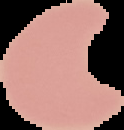
Image is 124×130 pixels. Result: negative for malaria parasites. The area outside the segmented cell region is set to black. From a thin blood film.